Assess this cell for malaria.
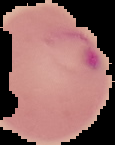
Parasitized.

{
  "preparation": "thin blood film",
  "image_type": "cell region segmented out of the field of view; surrounding area masked to black",
  "image_size": "115×145 pixels"
}